Report the malaria status of this cell.
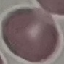
Uninfected.

stain = Giemsa
capture = smartphone through the microscope eyepiece
preparation = thin blood film
image type = automatically extracted cell patch, resized to 64 × 64 pixels